Point out every malaria parasite and every leukocyte.
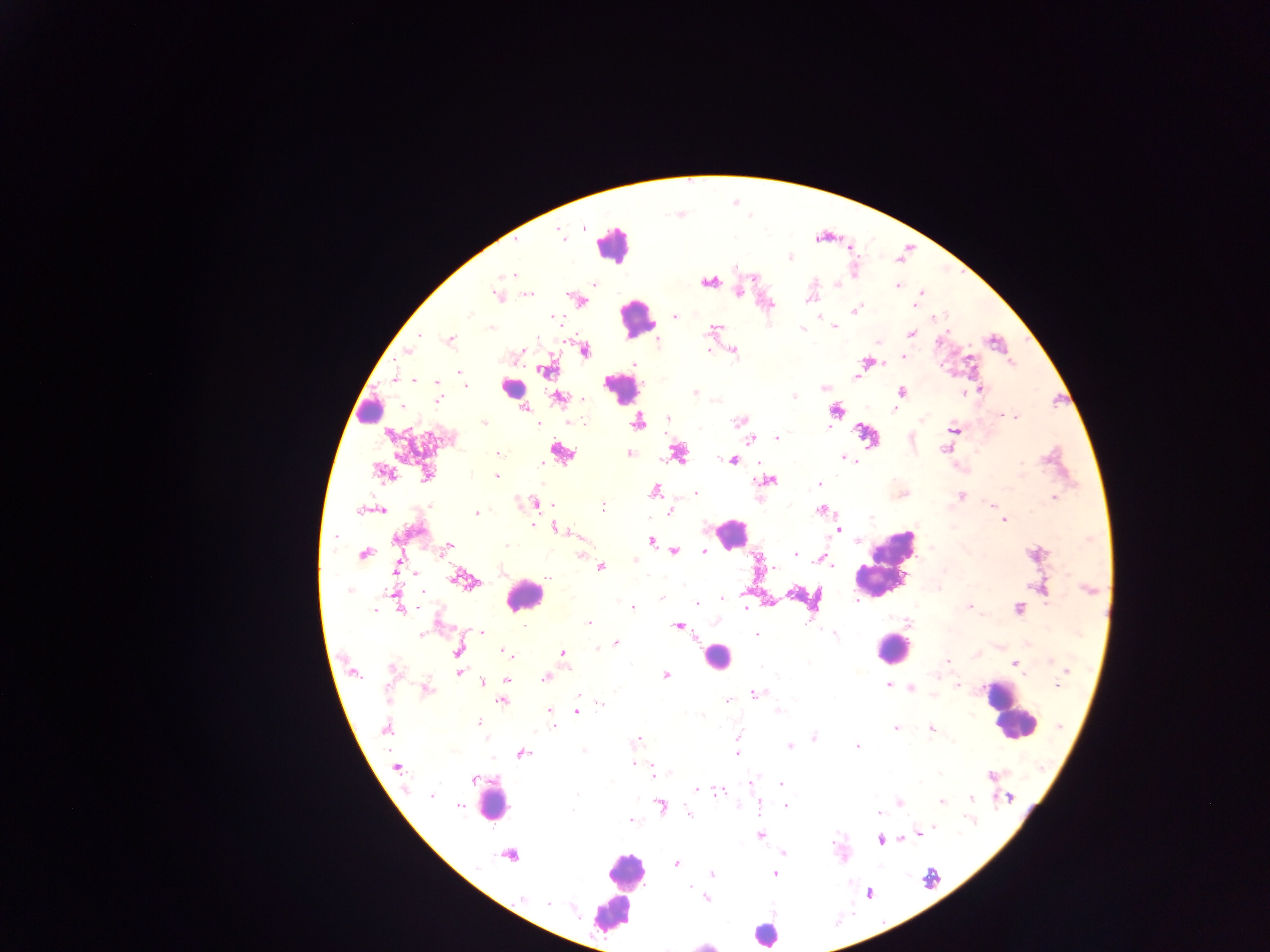

Approximate centers as [x, y] in pixels.
Malaria parasites: [583, 227], [560, 236], [789, 257], [736, 268], [511, 275], [708, 283], [594, 284], [838, 284], [898, 286], [738, 293], [920, 293], [497, 294], [529, 294], [808, 299], [916, 303], [855, 310], [470, 316], [675, 316], [558, 319], [492, 327], [834, 327], [714, 328], [802, 329], [911, 333], [420, 335], [450, 340], [878, 341], [708, 350], [408, 351], [584, 351], [735, 352], [518, 353], [904, 356], [867, 362], [546, 370], [460, 372], [395, 377], [856, 377], [415, 380], [437, 382], [464, 385], [825, 388], [982, 389], [902, 392], [694, 393], [963, 393], [794, 396], [558, 397], [582, 399], [438, 400], [524, 409], [894, 410], [1003, 416], [1015, 417], [668, 418], [921, 420], [571, 421], [738, 421], [637, 422], [484, 423], [538, 424], [953, 430], [388, 435], [776, 438], [751, 439], [945, 449], [561, 452], [498, 453], [629, 454], [678, 454], [844, 458], [733, 461], [541, 464], [381, 473], [427, 473], [496, 476], [769, 481], [820, 483], [654, 490], [696, 493], [961, 495], [1053, 498], [535, 503], [992, 506], [604, 507], [360, 511], [381, 511], [820, 511], [671, 512], [476, 513], [871, 518], [1004, 521], [533, 525], [556, 528], [838, 529], [335, 536], [580, 536], [651, 540], [858, 541], [506, 545], [447, 546], [674, 551], [704, 551], [581, 554], [796, 554], [364, 555], [820, 558], [634, 561], [826, 561], [831, 565], [602, 567], [774, 568], [416, 574], [547, 577], [458, 579], [939, 588], [349, 591], [423, 592], [394, 593], [661, 598], [723, 598], [856, 601], [696, 604], [970, 607], [633, 608], [746, 608], [1018, 608], [375, 610], [400, 610], [589, 623], [909, 623], [524, 626], [677, 626], [482, 632], [422, 635], [756, 635], [835, 635], [616, 643], [598, 648], [458, 650], [505, 651], [563, 653], [946, 660], [1051, 661], [1014, 663], [568, 668], [392, 669], [1068, 670], [458, 672], [353, 673], [1023, 675], [666, 676], [545, 678], [507, 679], [482, 683], [887, 685], [958, 685], [1057, 685], [910, 687], [426, 690], [757, 692], [932, 696], [579, 697], [728, 700], [503, 701], [601, 703], [549, 711], [577, 711], [778, 712], [702, 715], [478, 722], [551, 725], [1058, 726], [386, 728], [895, 728], [931, 729], [739, 736], [814, 737], [636, 740], [790, 746], [857, 746], [583, 751], [522, 754], [737, 754], [632, 763], [396, 767], [654, 772], [991, 776], [474, 780], [752, 781], [781, 784], [696, 790], [719, 792], [578, 794], [432, 795], [1010, 797], [972, 798], [941, 801], [899, 802], [759, 805], [458, 806], [660, 806], [786, 807], [574, 812], [878, 812], [688, 814], [630, 820], [932, 829], [919, 833], [760, 835], [879, 840], [782, 853], [676, 863], [713, 874], [775, 874], [690, 887], [522, 897], [706, 898], [548, 904].
Leukocytes: [612, 244], [636, 320], [511, 388], [621, 388], [371, 411], [731, 533], [887, 564], [524, 595], [892, 649], [716, 657], [1011, 712], [492, 802], [623, 871], [618, 891], [764, 934].

Summary:
  - Field of view: single
  - Capture: mobile-phone photograph through a microscope
  - Preparation: thick blood smear
  - Image size: 1270×952 pixels
  - Country: Ghana